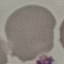

malaria status = uninfected
image type = automatically extracted cell patch, resized to 64 × 64 pixels
stain = Giemsa
capture = smartphone through the microscope eyepiece
preparation = thin smear